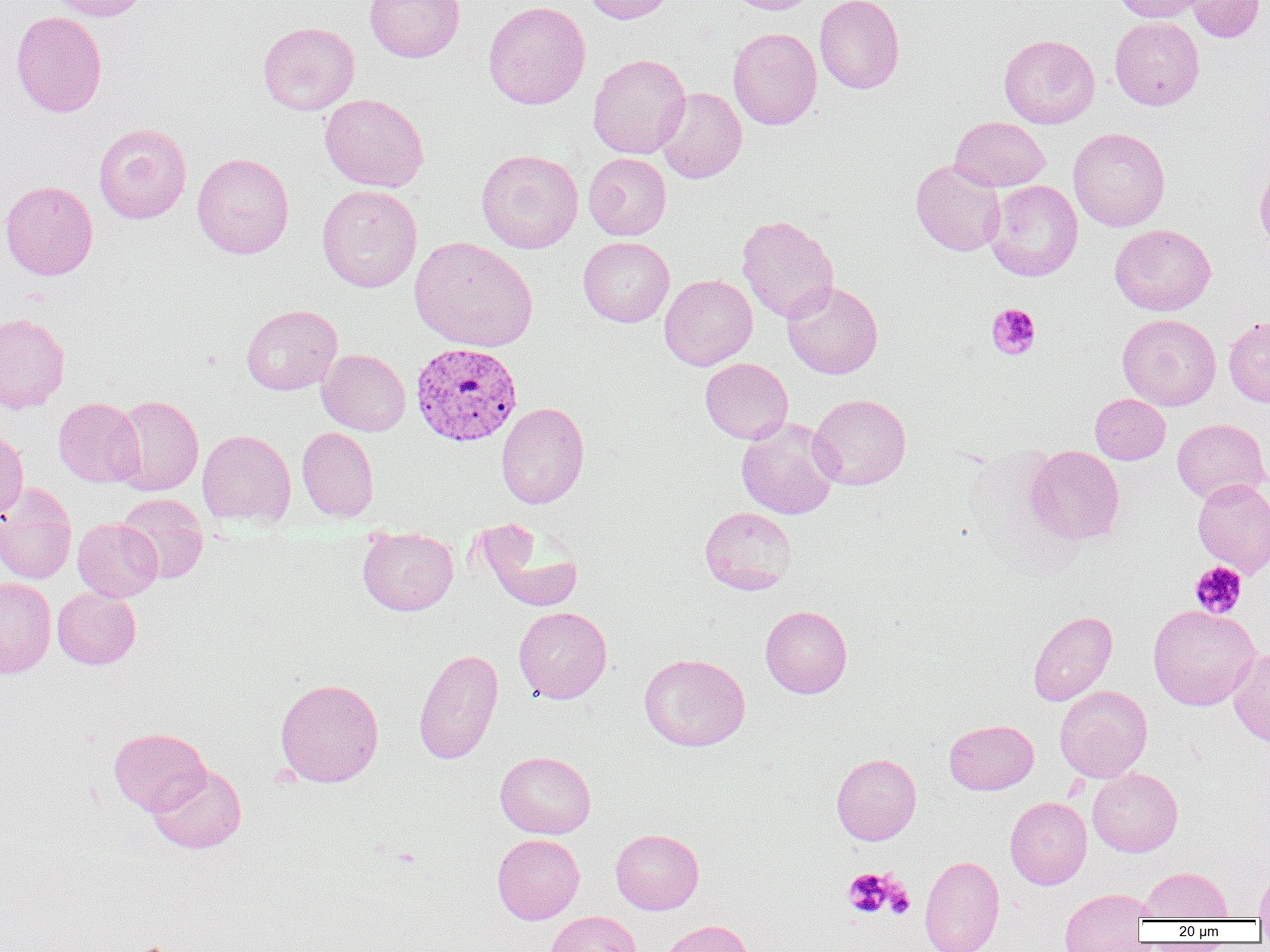

Approximate bounding boxes as [x1, y1, x2, y2] in pixels. Uninfected red blood cell locations: [45, 0, 148, 21], [365, 0, 465, 62], [582, 0, 678, 24], [726, 0, 819, 14], [814, 0, 905, 94], [1113, 0, 1213, 23], [1185, 0, 1266, 43], [483, 1, 590, 110], [10, 11, 107, 117], [1110, 16, 1205, 110], [258, 21, 359, 115], [728, 27, 822, 130], [998, 34, 1100, 128], [588, 53, 691, 159], [656, 87, 747, 183], [320, 93, 429, 192], [950, 117, 1050, 192], [93, 122, 192, 224], [1068, 127, 1170, 232], [477, 149, 584, 253], [583, 152, 671, 240], [192, 153, 294, 259], [911, 159, 1006, 256], [1255, 162, 1270, 255], [0, 179, 98, 280], [985, 180, 1083, 281], [317, 185, 422, 292], [736, 215, 839, 323], [1109, 224, 1216, 316], [409, 236, 538, 352], [578, 236, 675, 326], [660, 274, 757, 370], [782, 280, 883, 379], [241, 304, 342, 395], [0, 312, 71, 413], [1118, 314, 1221, 410], [1224, 316, 1270, 407], [317, 349, 410, 435], [700, 358, 793, 444], [808, 393, 911, 490], [1090, 394, 1170, 464], [112, 395, 204, 496], [53, 397, 144, 487], [496, 402, 589, 509], [736, 417, 840, 519], [1172, 418, 1269, 503], [0, 427, 29, 521], [297, 427, 379, 522], [197, 429, 296, 527], [1026, 445, 1125, 544], [1192, 478, 1270, 577], [0, 485, 77, 584], [116, 493, 208, 584], [700, 506, 797, 595], [73, 517, 162, 601], [476, 520, 583, 612], [358, 525, 458, 615], [0, 577, 56, 678], [53, 587, 141, 669], [1148, 604, 1260, 710], [760, 605, 852, 698], [514, 606, 612, 703], [1027, 610, 1117, 706], [1227, 647, 1270, 747], [413, 648, 504, 764], [639, 653, 750, 751], [275, 678, 384, 787], [1055, 685, 1152, 782], [944, 719, 1038, 795], [109, 727, 211, 815], [495, 751, 596, 839], [831, 753, 921, 845], [148, 763, 246, 854], [1087, 768, 1183, 857], [1005, 796, 1092, 889], [611, 828, 704, 914], [492, 834, 584, 924], [920, 854, 1004, 952], [1254, 866, 1270, 922], [1143, 867, 1232, 921], [1059, 888, 1154, 951], [545, 910, 642, 952], [657, 919, 755, 952]. Platelet locations: [986, 303, 1041, 359], [1189, 561, 1247, 619], [844, 868, 899, 918], [884, 884, 915, 918]. Plasmodium vivax-infected red blood cell locations: [410, 342, 523, 446]. Slide-level diagnosis: Plasmodium vivax. 1000x magnification. Single field of view. Thin blood film. Image is 1270×952 pixels. Optical microscopy.